State the blood parasite species.
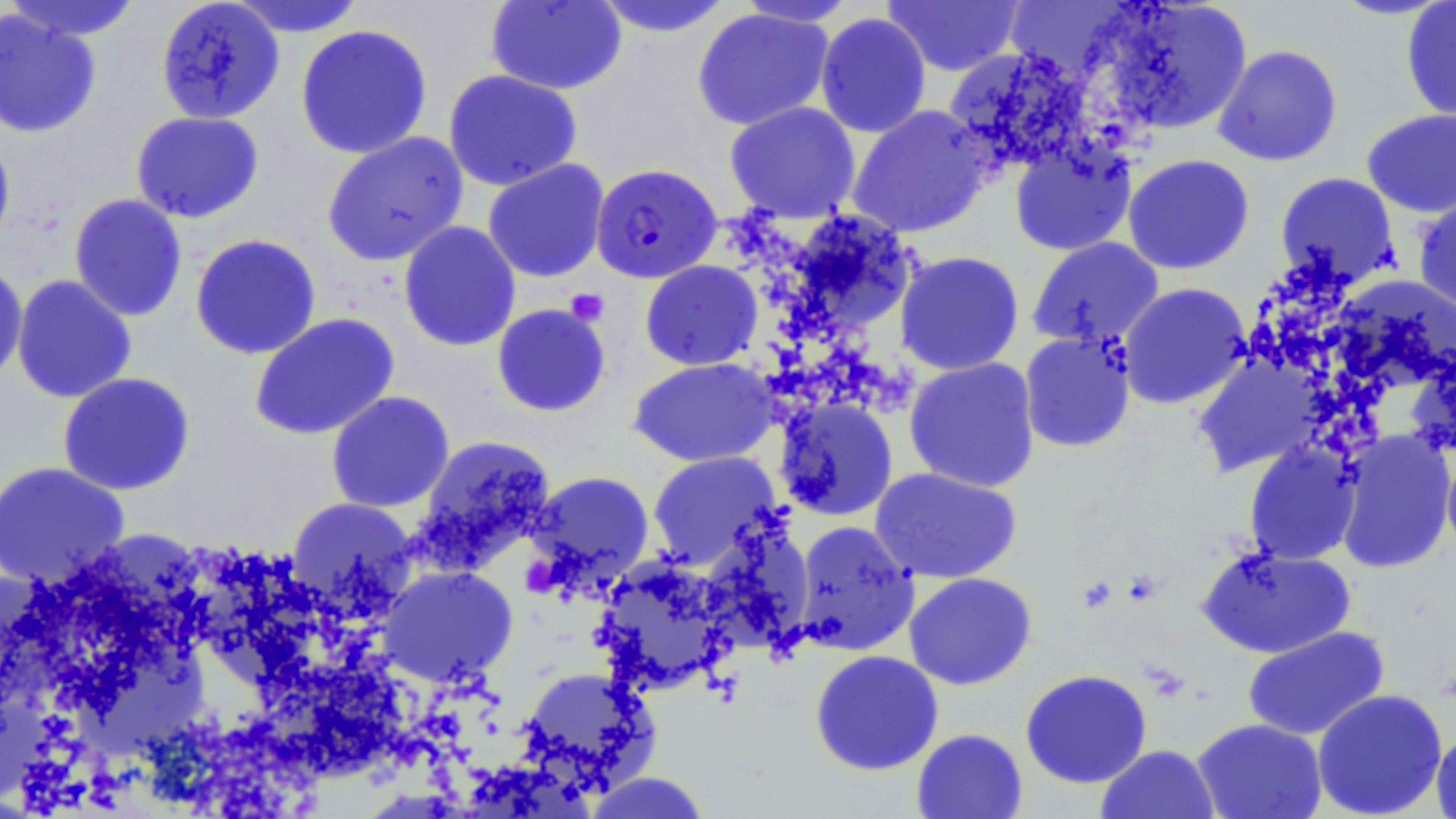
Plasmodium falciparum.

Approximate bounding boxes as (x1, y1, x2, y2) in pixels. Uninfected red blood cell locations: (3, 0, 145, 42), (226, 0, 368, 37), (1091, 0, 1253, 137), (155, 1, 285, 125), (486, 1, 627, 94), (590, 1, 736, 38), (732, 1, 860, 27), (882, 1, 1024, 76), (1400, 1, 1456, 124), (1002, 2, 1144, 84), (0, 8, 101, 139), (691, 8, 835, 131), (815, 13, 931, 138), (294, 24, 433, 160), (1212, 44, 1343, 167), (942, 46, 1096, 174), (443, 69, 583, 191), (724, 102, 861, 222), (847, 105, 992, 239), (1361, 109, 1456, 218), (130, 111, 265, 223), (0, 127, 16, 257), (321, 131, 469, 267), (1010, 138, 1138, 256), (1122, 153, 1255, 275), (482, 159, 610, 283), (1275, 172, 1402, 290), (1413, 191, 1456, 318), (68, 194, 188, 321), (779, 210, 920, 342), (398, 220, 521, 352), (190, 233, 321, 360), (1027, 237, 1163, 349), (895, 251, 1024, 376), (0, 260, 28, 388), (640, 260, 763, 371), (12, 274, 137, 404), (1118, 282, 1252, 409), (491, 303, 612, 418), (248, 312, 400, 441), (1018, 330, 1137, 453), (1192, 354, 1328, 477), (904, 357, 1041, 493), (629, 358, 779, 468), (57, 372, 196, 496), (326, 391, 455, 513), (774, 397, 898, 522), (1334, 431, 1455, 574), (413, 434, 556, 571), (1440, 439, 1456, 561), (1244, 442, 1361, 565), (646, 451, 783, 570), (0, 461, 130, 589), (870, 467, 1022, 584), (526, 470, 655, 593), (285, 497, 420, 621), (696, 520, 816, 656), (793, 521, 920, 656), (1197, 543, 1355, 658), (592, 556, 735, 695), (377, 565, 519, 687), (903, 572, 1037, 690), (1242, 626, 1389, 741), (809, 649, 944, 776), (517, 666, 661, 794), (1020, 669, 1152, 789), (1312, 688, 1448, 818), (1192, 718, 1327, 819), (1431, 727, 1456, 819), (911, 728, 1028, 819), (1095, 744, 1220, 819), (584, 771, 712, 819). Plasmodium falciparum-infected red blood cell locations: (593, 163, 724, 283). Platelet locations: (565, 288, 609, 325), (524, 562, 564, 599), (1122, 568, 1163, 606), (1077, 575, 1119, 615). Light microscopy. Thin blood smear. Single field of view. May-Grünwald-Giemsa-stained preparation. 1000x magnification. Image is 1456×819 pixels.